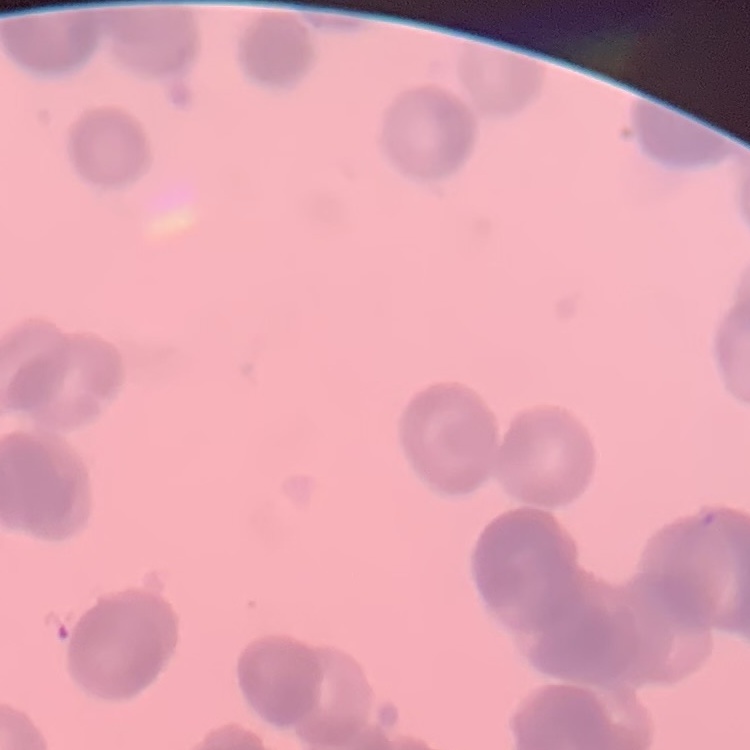

erythrocyte_morphology: rouleaux formation
preparation: thin blood film
image_type: one tile cut from a larger photomicrograph
stain: Field's or Giemsa